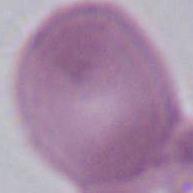

identification = red blood cell
magnification = 1000x
modality = micrograph